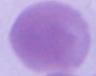

Summary:
  - Magnification: 1000x
  - Identification: erythrocyte
  - Modality: micrograph